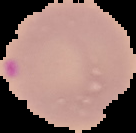
image size = 136×133 pixels
result = malaria parasites detected
image type = segmented cell region on a black background
preparation = thin blood film